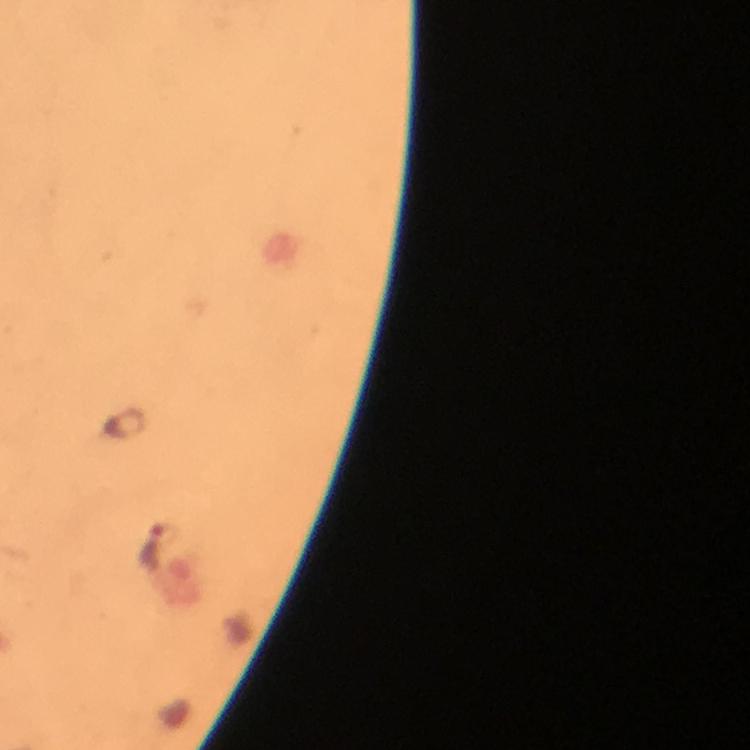
capture: smartphone mounted on the microscope
immersion_oil: used
context: from a diagnostic examination for malaria
preparation: thick blood smear
plasmodium_parasite_locations: 'approximate centers as [x, y] in pixels: [151, 543]'
image_size: 750×750 pixels
cropped_from: a single field of view
magnification: 100x
stain: Giemsa